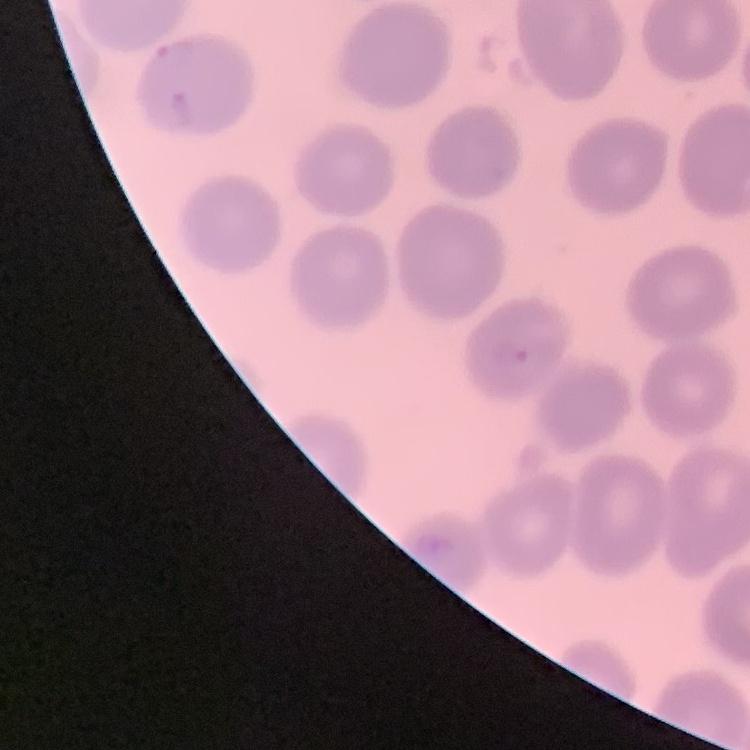
Summary:
  - Erythrocyte morphology: no rouleaux formation
  - Preparation: thin peripheral smear
  - Stain: Field's or Giemsa
  - Image type: square crop of a larger photomicrograph